Assess this cell for malaria.
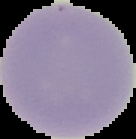

Uninfected.

image type = segmented cell region on a black background
image size = 136×139 pixels
preparation = thin blood film